Name the parasite shown.
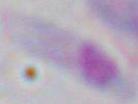
This is Toxoplasma gondii.

magnification: 1000x
modality: photomicrograph